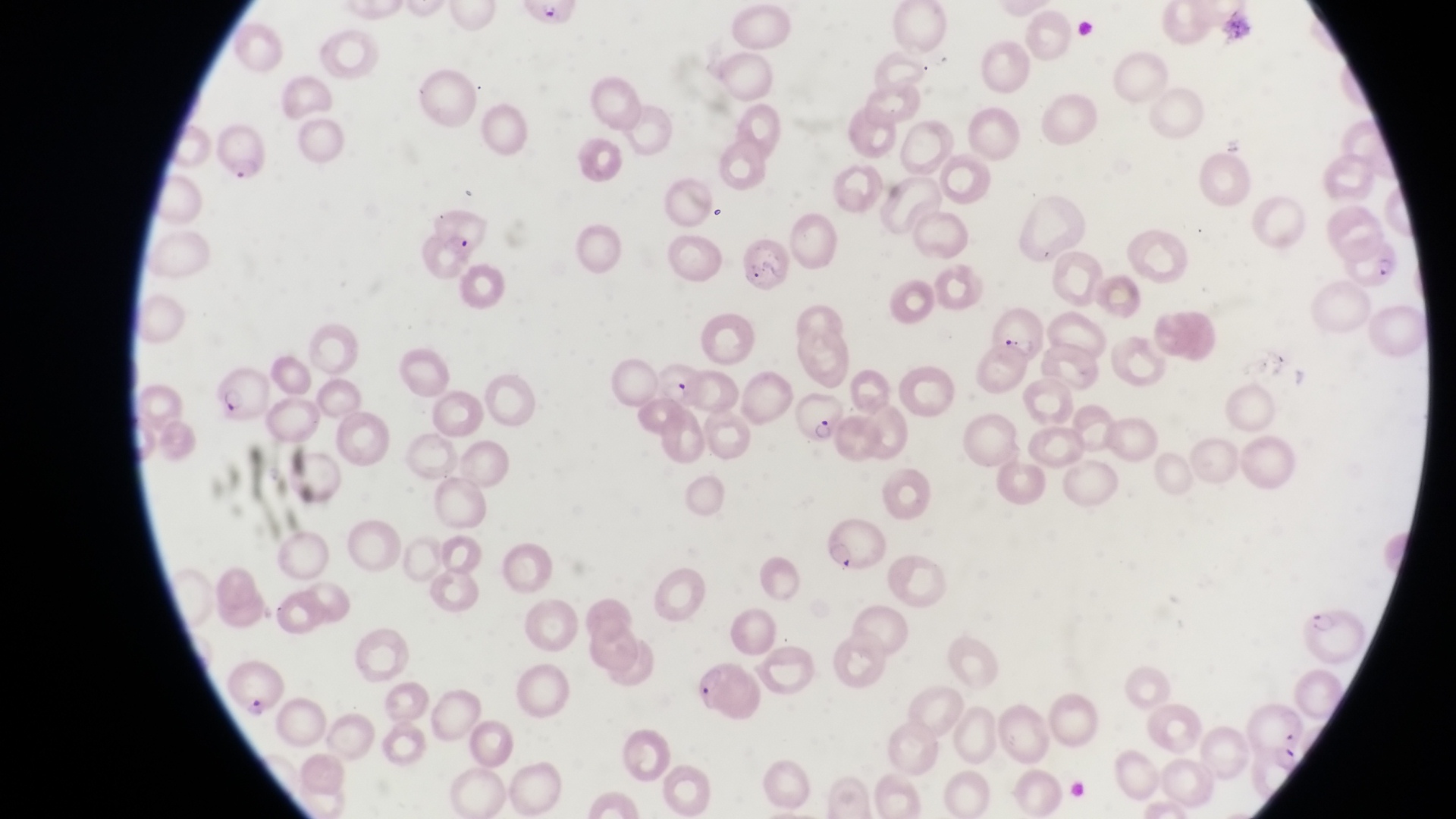 Approximate bounding boxes as (left, top, right, bottom) in pixels. Parasitised red blood cell locations: (214, 124, 275, 188), (426, 209, 489, 259), (1348, 232, 1406, 296), (739, 237, 798, 303), (990, 309, 1042, 365), (650, 356, 702, 414), (211, 362, 271, 420), (788, 386, 841, 446), (814, 513, 886, 572), (1304, 592, 1365, 656), (686, 658, 763, 724). Image is 1456×819 pixels. Photographed through the eyepiece of an Olympus CX-23 microscope with a smartphone camera. Sample from Uganda. Single field of view. Thin blood smear. At a magnification of 1000x.